Classify this cell by malaria status.
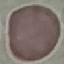

It is uninfected.

Giemsa stain. Photographed with a smartphone camera at the microscope eyepiece. Thin blood film. Automatically extracted cell patch, resized to 64 × 64 pixels.